Name the blood parasite species.
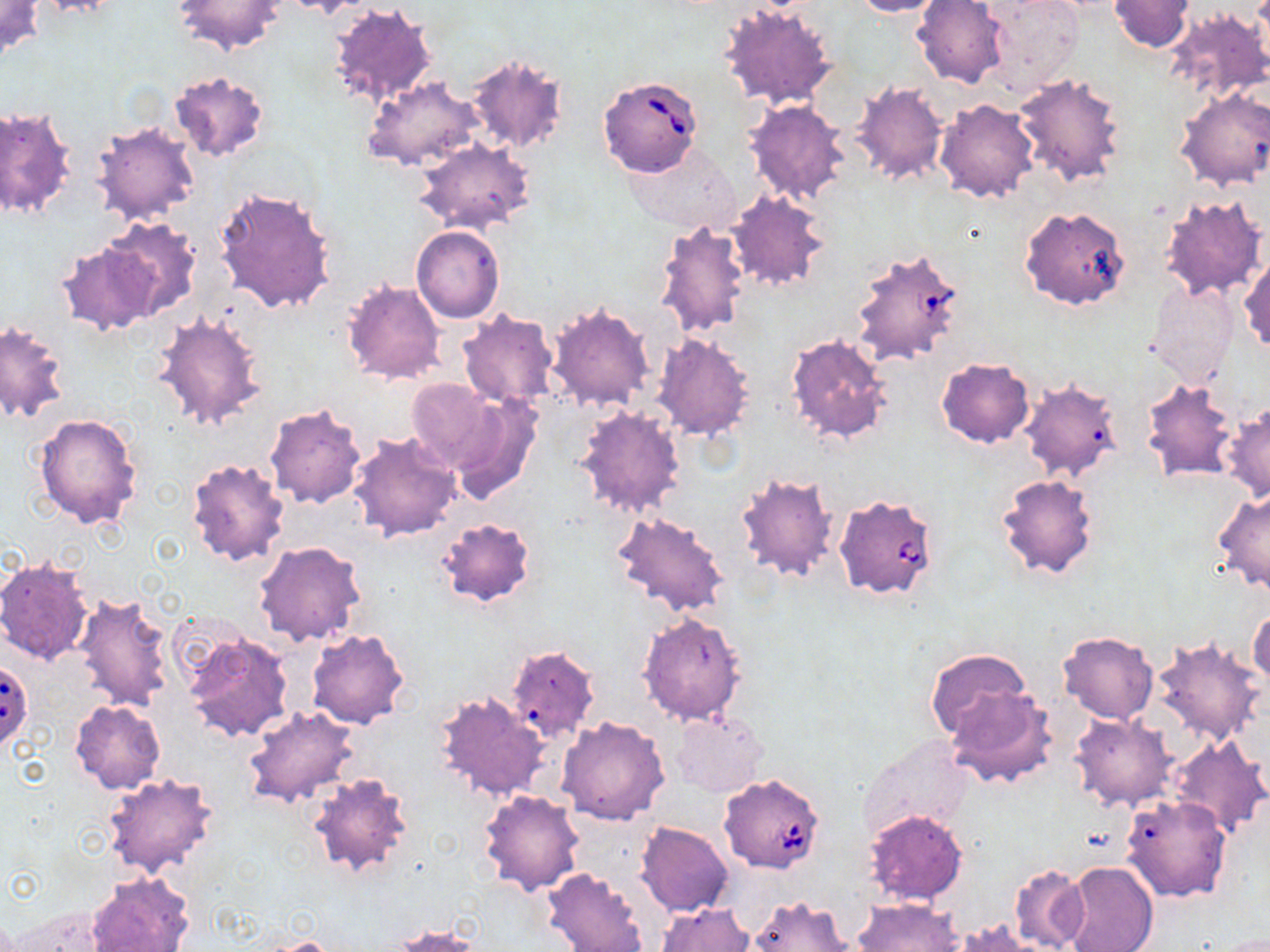

Babesia divergens.

field of view = single
image size = 1270×952 pixels
preparation = thin blood film
stain = May-Grünwald-Giemsa
modality = optical microscopy
magnification = 1000x
Babesia divergens-infected red blood cell locations = approximate bounding boxes as (x1,y1)-(x2,y2) corner pairs in pixels: (597,75)-(704,176), (849,247)-(965,369), (835,493)-(939,600), (0,660)-(34,751), (718,773)-(825,873)
uninfected red blood cell locations = approximate bounding boxes as (x1,y1)-(x2,y2) corner pairs in pixels: (0,0)-(44,59), (34,0)-(125,18), (172,0)-(285,54), (849,0)-(947,17), (913,0)-(1009,88), (980,0)-(1082,94), (1109,0)-(1196,53), (720,2)-(840,112), (329,5)-(436,109), (1163,7)-(1270,106), (465,52)-(569,155), (167,71)-(270,163), (1012,72)-(1127,188), (362,76)-(484,172), (848,80)-(950,188), (1173,86)-(1269,191), (935,99)-(1039,202), (744,100)-(854,204), (1,106)-(75,220), (91,120)-(199,225), (411,137)-(537,237), (628,142)-(741,234), (211,186)-(339,315), (726,191)-(830,292), (1159,194)-(1268,304), (1021,211)-(1130,314), (102,216)-(201,318), (654,218)-(755,338), (411,225)-(504,323), (57,241)-(156,335), (1240,254)-(1269,353), (340,277)-(446,385), (1146,282)-(1239,388), (546,302)-(655,413), (457,309)-(558,409), (151,310)-(268,432), (0,320)-(70,424), (653,331)-(758,441), (785,332)-(892,446), (935,357)-(1035,448), (1020,377)-(1124,482), (405,378)-(503,475), (1142,379)-(1239,483), (450,395)-(542,505), (264,402)-(366,509), (1224,402)-(1270,503), (574,404)-(688,519), (33,412)-(144,531), (348,430)-(463,542), (185,457)-(291,568), (735,469)-(842,584), (995,473)-(1098,581), (1213,489)-(1270,594), (610,510)-(733,619), (435,515)-(538,608), (254,540)-(367,646), (0,556)-(94,666), (71,592)-(175,713), (1248,606)-(1270,693), (637,612)-(748,727), (179,628)-(294,745), (306,628)-(410,728), (1057,631)-(1157,724), (1152,635)-(1265,746), (509,644)-(595,740), (924,648)-(1032,742), (945,685)-(1057,789), (434,690)-(548,801), (70,699)-(166,794), (243,706)-(359,808), (672,711)-(767,797), (1069,713)-(1178,810), (556,716)-(670,825), (857,735)-(972,844), (1166,736)-(1268,837), (306,771)-(416,877), (103,772)-(218,880), (479,789)-(586,895), (1121,794)-(1231,902), (864,810)-(969,906), (636,821)-(734,918), (1060,861)-(1159,952), (1010,865)-(1088,951), (542,868)-(648,952), (87,872)-(192,952), (746,894)-(857,952), (855,899)-(964,952), (657,902)-(755,952), (12,904)-(119,952), (954,920)-(1050,951), (390,924)-(483,951), (254,936)-(343,951)